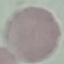

malaria status = uninfected
preparation = thin blood smear
image type = cell patch, automatically extracted from a larger field of view and resized to 64 × 64 pixels
capture = smartphone through the microscope eyepiece
stain = Giemsa